Classify this cell by malaria status.
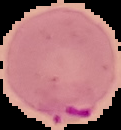

It is parasitized.

Summary:
  - Preparation: thin blood film
  - Image type: segmented cell region with the area outside set to black
  - Image size: 121×130 pixels